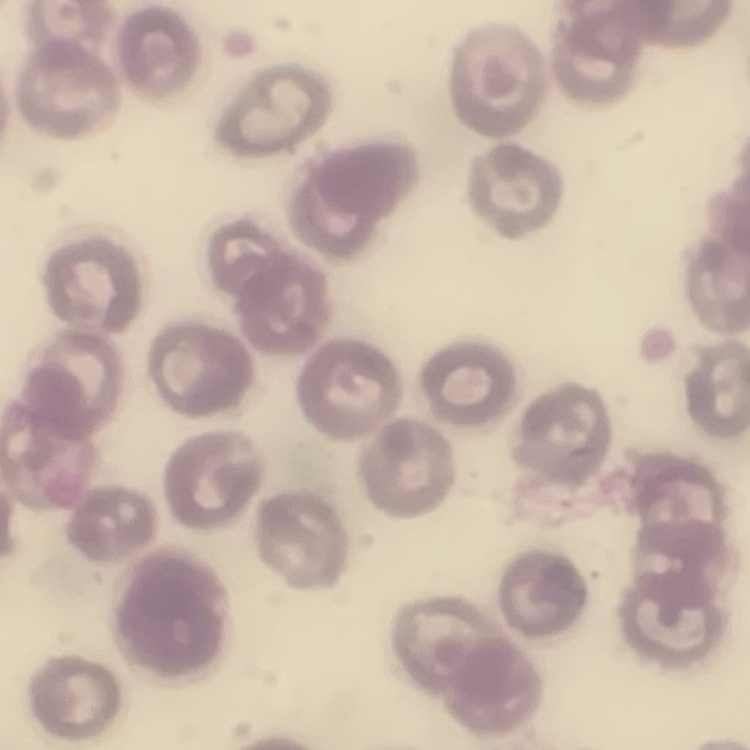

The red blood cells show no rouleaux formation. Square crop of a larger photomicrograph. Field's or Giemsa stain. Thin peripheral smear.